Evaluate for Plasmodium parasites.
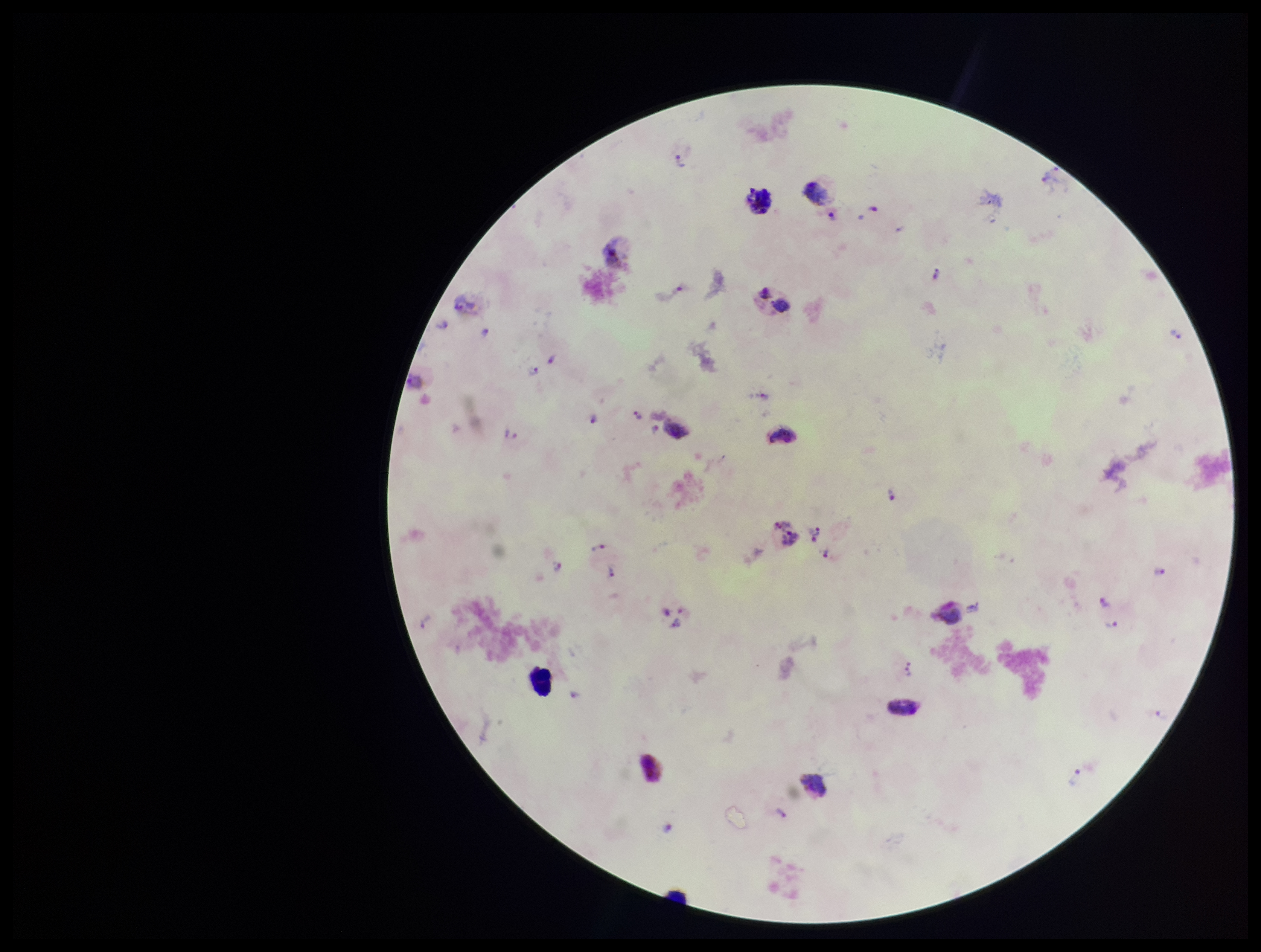

Seen.

Preparation: thick. Image is 1261×952 pixels. Single field of view. Patient malaria status: infected. Leukocyte count: 3. Species reported for this patient: Plasmodium vivax. Parasite count: 25. Giemsa stain. Photographed through the microscope eyepiece with a smartphone camera.